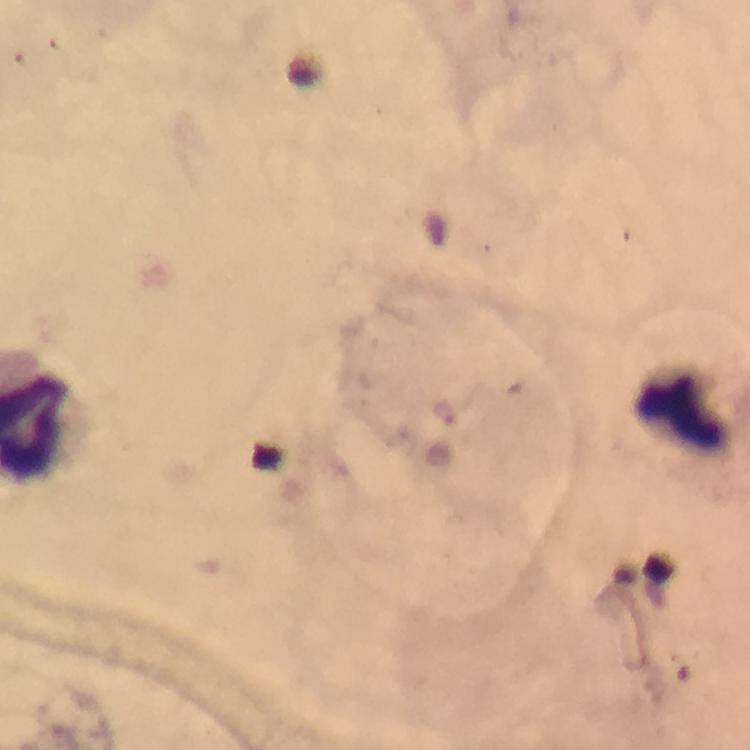

Approximate centers as {x, y} in pixels. Malaria parasite locations: {445, 415}. Leukocyte locations: {678, 415}. At 100x magnification. Thick smear. Image is 750×750 pixels. Cropped region of a single field of view. Giemsa-stained preparation. Photographed through the microscope with a smartphone camera. Immersion oil was used. From a diagnostic examination for malaria.